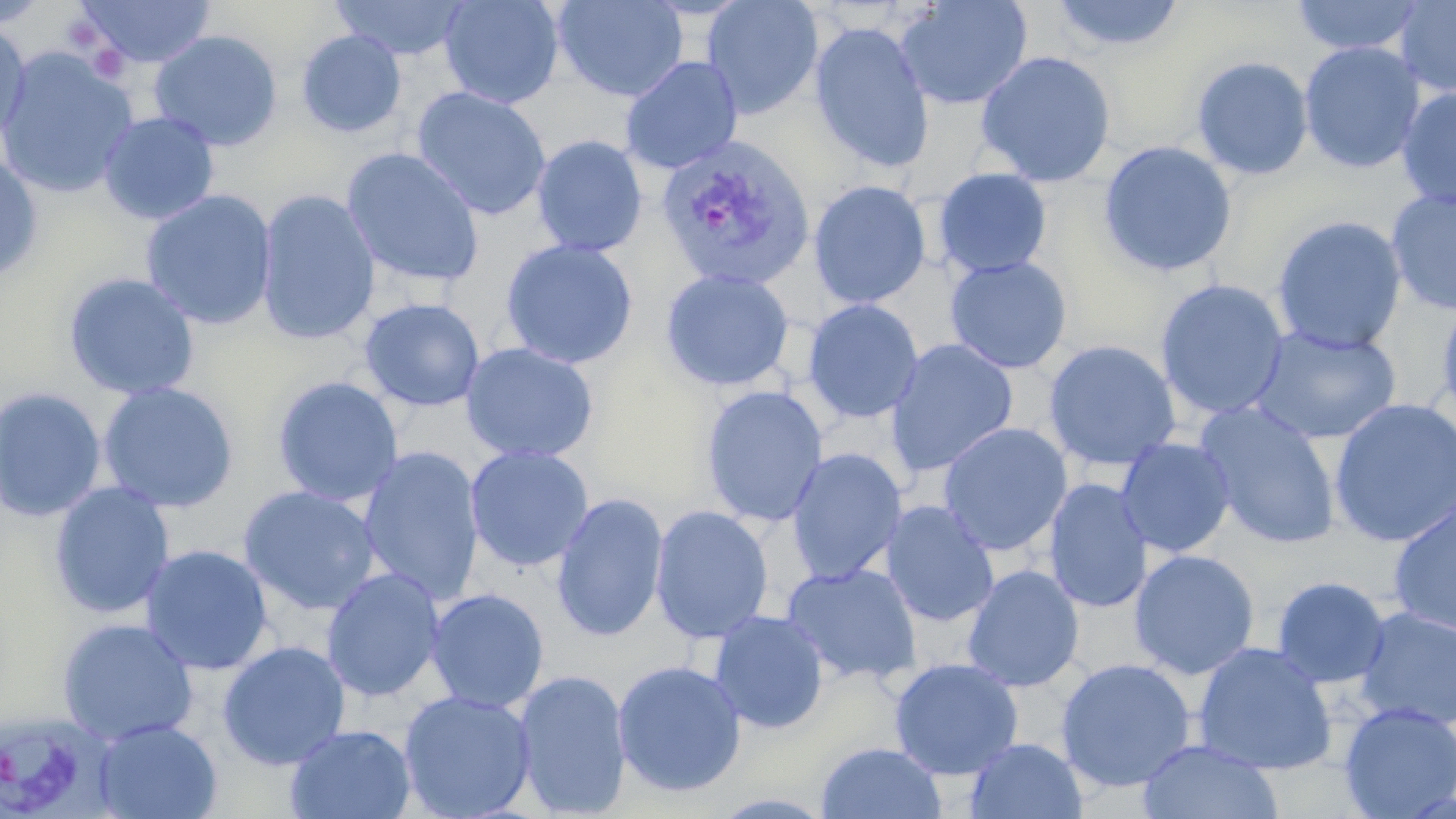
slide-level diagnosis = Plasmodium vivax
preparation = thin blood film
Plasmodium vivax-infected red blood cell locations = approximate bounding boxes as (x1,y1)-(x2,y2) corner pairs in pixels: (656,135)-(816,292), (0,710)-(114,819)
image size = 1456×819 pixels
field of view = one of a larger specimen
magnification = 1000x
modality = optical microscopy
stain = May-Grünwald-Giemsa
uninfected red blood cell locations = approximate bounding boxes as (x1,y1)-(x2,y2) corner pairs in pixels: (0,0)-(50,30), (75,0)-(216,68), (331,0)-(472,61), (439,0)-(565,109), (552,0)-(688,102), (701,0)-(824,119), (895,0)-(1033,111), (1049,0)-(1186,53), (1290,0)-(1428,57), (1394,0)-(1456,98), (0,20)-(32,146), (809,21)-(935,173), (296,29)-(406,138), (149,30)-(283,151), (1298,41)-(1425,174), (0,47)-(140,201), (975,50)-(1116,187), (1191,55)-(1314,181), (620,56)-(743,174), (411,86)-(552,221), (1396,86)-(1456,212), (98,111)-(220,225), (531,135)-(648,257), (1098,140)-(1237,278), (341,147)-(486,288), (0,153)-(44,284), (933,167)-(1053,278), (808,179)-(931,310), (256,188)-(380,347), (1385,188)-(1456,316), (140,189)-(277,330), (1271,214)-(1408,354), (499,238)-(639,369), (944,255)-(1073,374), (659,268)-(795,392), (62,271)-(200,401), (1154,278)-(1290,420), (1434,294)-(1456,426), (359,297)-(484,412), (801,298)-(924,424), (1249,324)-(1403,445), (885,339)-(1019,476), (1043,339)-(1182,471), (460,342)-(600,463), (272,376)-(404,507), (97,381)-(240,513), (700,385)-(828,527), (0,387)-(106,522), (1328,398)-(1456,548), (1195,402)-(1342,549), (937,422)-(1072,557), (1116,437)-(1236,557), (464,445)-(594,572), (357,446)-(484,607), (786,448)-(908,585), (1043,478)-(1153,614), (48,481)-(176,619), (237,485)-(381,615), (551,493)-(668,643), (1387,493)-(1456,637), (880,500)-(1000,627), (650,504)-(774,644), (139,544)-(274,675), (1129,549)-(1260,680), (781,562)-(922,686), (962,564)-(1084,693), (320,568)-(446,702), (1271,576)-(1392,689), (426,588)-(550,713), (1353,606)-(1456,732), (708,609)-(829,734), (56,617)-(199,746), (217,640)-(351,770), (1192,641)-(1338,775), (889,657)-(1024,780), (1056,657)-(1197,793), (611,659)-(748,798), (513,669)-(632,818), (399,689)-(537,819), (1338,701)-(1456,818), (92,718)-(222,819), (284,724)-(417,819), (964,737)-(1088,819), (1137,739)-(1282,819), (814,741)-(947,819)